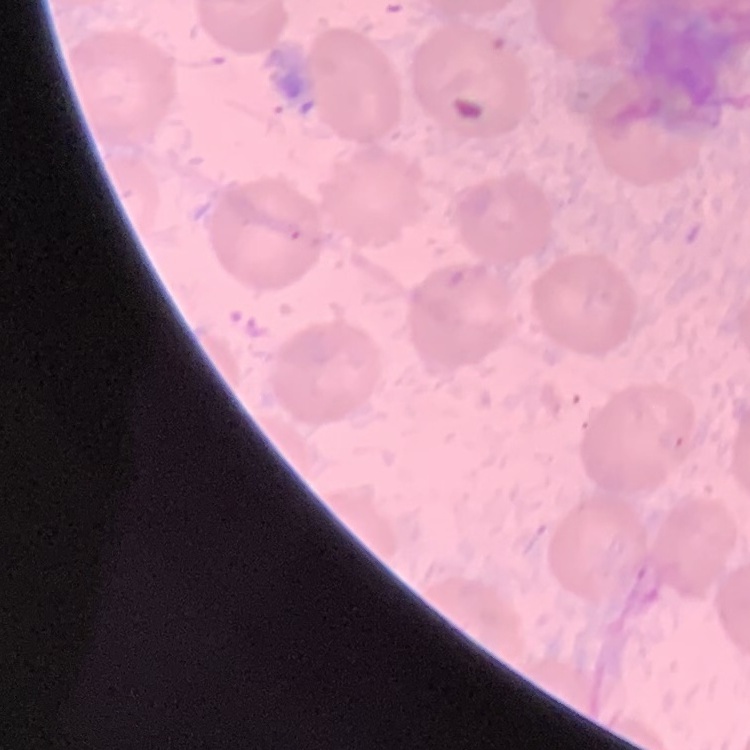
Summary:
  - Red blood cell morphology: no rouleaux formation
  - Image type: one tile cut from a larger photomicrograph
  - Preparation: thin blood smear
  - Stain: Field's or Giemsa